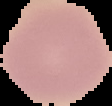
Segmented cell region on a black background. Result: negative for malaria parasites. From a thin blood smear. Image is 112×106 pixels.